Describe the morphology of the red blood cells.
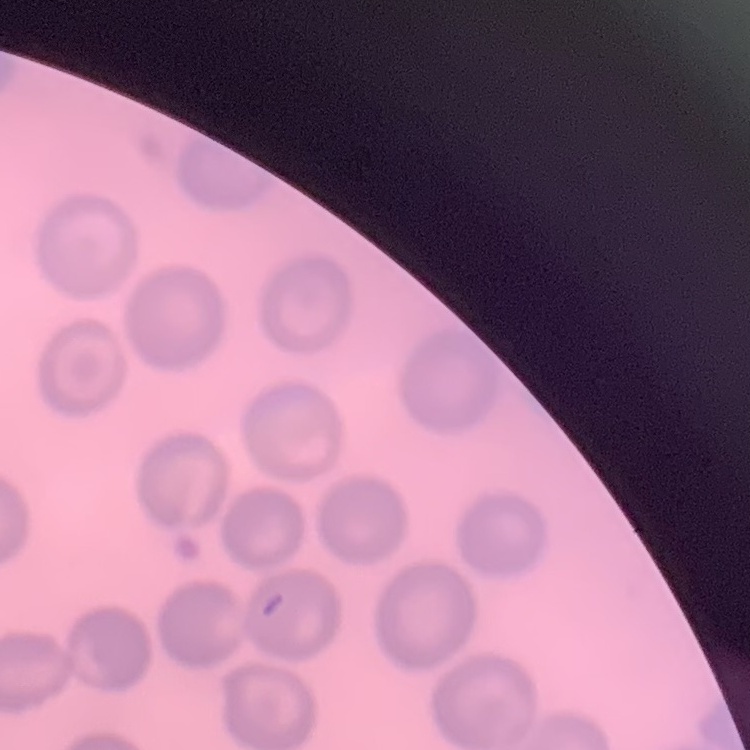
No rouleaux formation.

Square crop of a larger photomicrograph. Thin blood smear. Stained with either Field's or Giemsa.